State which parasite is depicted.
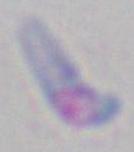

This is Toxoplasma gondii.

Photomicrograph. Captured at 1000x magnification.